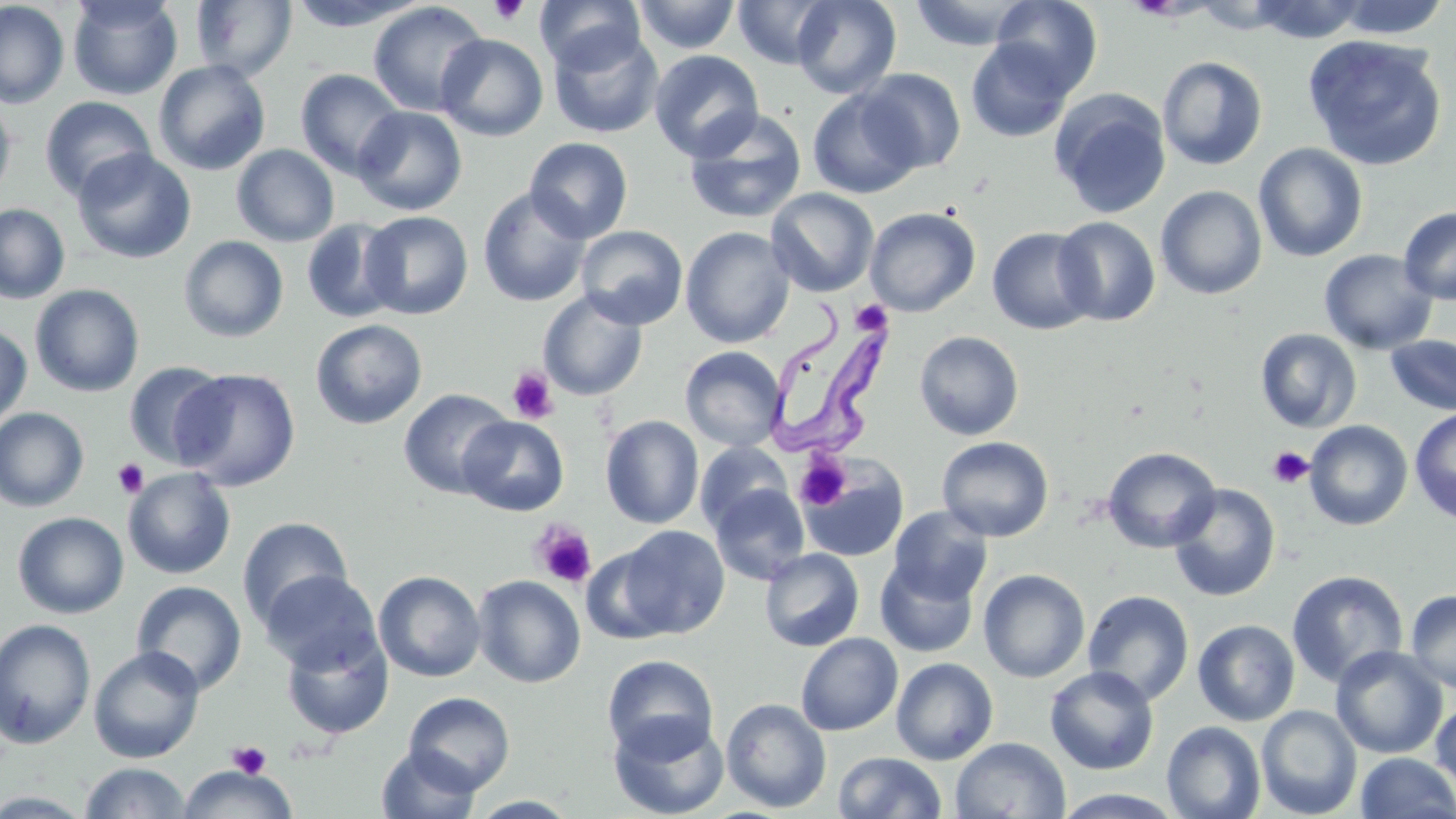

{
  "slide_level_diagnosis": "Trypanosoma brucei",
  "field_of_view": "one of a larger specimen",
  "stain": "May-Grünwald-Giemsa",
  "trypanosoma_brucei_locations": "approximate bounding boxes as named x1/y1/x2/y2 corners in pixels: (x1=768, y1=302, x2=894, y2=456)",
  "platelet_locations": "approximate bounding boxes as named x1/y1/x2/y2 corners in pixels: (x1=488, y1=0, x2=529, y2=25), (x1=850, y1=299, x2=893, y2=336), (x1=507, y1=368, x2=558, y2=423), (x1=1267, y1=446, x2=1314, y2=489), (x1=793, y1=453, x2=852, y2=511), (x1=112, y1=458, x2=150, y2=499), (x1=530, y1=521, x2=597, y2=589), (x1=227, y1=741, x2=271, y2=778)",
  "uninfected_red_blood_cell_locations": "approximate bounding boxes as named x1/y1/x2/y2 corners in pixels: (x1=67, y1=0, x2=183, y2=100), (x1=287, y1=0, x2=428, y2=31), (x1=535, y1=0, x2=645, y2=74), (x1=633, y1=0, x2=741, y2=54), (x1=732, y1=0, x2=837, y2=69), (x1=791, y1=0, x2=901, y2=98), (x1=991, y1=0, x2=1103, y2=96), (x1=1248, y1=0, x2=1369, y2=44), (x1=1333, y1=0, x2=1451, y2=40), (x1=0, y1=1, x2=70, y2=109), (x1=191, y1=1, x2=297, y2=82), (x1=908, y1=1, x2=1033, y2=50), (x1=368, y1=2, x2=489, y2=117), (x1=548, y1=26, x2=664, y2=139), (x1=436, y1=34, x2=548, y2=141), (x1=1302, y1=35, x2=1448, y2=170), (x1=965, y1=38, x2=1074, y2=143), (x1=649, y1=50, x2=764, y2=161), (x1=1157, y1=56, x2=1268, y2=170), (x1=153, y1=60, x2=271, y2=176), (x1=295, y1=69, x2=406, y2=180), (x1=857, y1=69, x2=967, y2=174), (x1=807, y1=88, x2=924, y2=199), (x1=1049, y1=89, x2=1172, y2=219), (x1=0, y1=95, x2=16, y2=201), (x1=39, y1=96, x2=156, y2=201), (x1=353, y1=106, x2=466, y2=215), (x1=683, y1=109, x2=808, y2=224), (x1=525, y1=137, x2=633, y2=243), (x1=1253, y1=143, x2=1369, y2=262), (x1=232, y1=144, x2=339, y2=247), (x1=72, y1=149, x2=196, y2=263), (x1=1155, y1=185, x2=1268, y2=300), (x1=477, y1=187, x2=591, y2=307), (x1=766, y1=188, x2=879, y2=297), (x1=0, y1=203, x2=70, y2=304), (x1=1399, y1=206, x2=1456, y2=304), (x1=864, y1=207, x2=980, y2=316), (x1=361, y1=211, x2=473, y2=320), (x1=1053, y1=215, x2=1161, y2=327), (x1=301, y1=218, x2=404, y2=324), (x1=576, y1=225, x2=688, y2=330), (x1=680, y1=227, x2=795, y2=348), (x1=987, y1=227, x2=1100, y2=335), (x1=179, y1=236, x2=289, y2=342), (x1=1319, y1=249, x2=1438, y2=354), (x1=30, y1=284, x2=145, y2=397), (x1=537, y1=290, x2=648, y2=401), (x1=311, y1=319, x2=428, y2=430), (x1=0, y1=323, x2=32, y2=430), (x1=1254, y1=328, x2=1362, y2=433), (x1=914, y1=331, x2=1024, y2=441), (x1=1385, y1=333, x2=1456, y2=416), (x1=680, y1=346, x2=787, y2=452), (x1=123, y1=362, x2=231, y2=469), (x1=172, y1=367, x2=301, y2=491), (x1=398, y1=389, x2=515, y2=499), (x1=0, y1=408, x2=90, y2=512), (x1=1409, y1=408, x2=1456, y2=524), (x1=458, y1=415, x2=569, y2=516), (x1=601, y1=415, x2=704, y2=529), (x1=1303, y1=420, x2=1413, y2=530), (x1=937, y1=436, x2=1054, y2=542), (x1=695, y1=442, x2=792, y2=532), (x1=1102, y1=446, x2=1222, y2=553), (x1=800, y1=458, x2=908, y2=563), (x1=122, y1=468, x2=236, y2=579), (x1=1168, y1=483, x2=1281, y2=603), (x1=709, y1=484, x2=810, y2=585), (x1=888, y1=506, x2=993, y2=605), (x1=13, y1=511, x2=129, y2=619), (x1=237, y1=516, x2=354, y2=631), (x1=611, y1=525, x2=730, y2=639), (x1=760, y1=548, x2=864, y2=651), (x1=875, y1=559, x2=979, y2=658), (x1=259, y1=569, x2=382, y2=673), (x1=978, y1=569, x2=1090, y2=683), (x1=1286, y1=569, x2=1409, y2=689), (x1=373, y1=570, x2=486, y2=682), (x1=473, y1=575, x2=586, y2=688), (x1=131, y1=580, x2=247, y2=696), (x1=1404, y1=588, x2=1456, y2=694), (x1=1082, y1=590, x2=1195, y2=705), (x1=0, y1=618, x2=96, y2=749), (x1=1192, y1=619, x2=1301, y2=726), (x1=280, y1=626, x2=394, y2=740), (x1=796, y1=633, x2=903, y2=735), (x1=89, y1=645, x2=205, y2=763), (x1=1331, y1=646, x2=1448, y2=759), (x1=601, y1=654, x2=719, y2=761), (x1=891, y1=657, x2=999, y2=765), (x1=1044, y1=666, x2=1159, y2=774), (x1=403, y1=691, x2=515, y2=794), (x1=1431, y1=696, x2=1456, y2=792), (x1=721, y1=698, x2=832, y2=813), (x1=1256, y1=705, x2=1362, y2=818), (x1=608, y1=713, x2=729, y2=819), (x1=1162, y1=720, x2=1266, y2=819), (x1=950, y1=736, x2=1070, y2=819), (x1=376, y1=746, x2=481, y2=819), (x1=833, y1=751, x2=947, y2=818), (x1=1355, y1=752, x2=1455, y2=818), (x1=80, y1=761, x2=192, y2=818), (x1=178, y1=767, x2=298, y2=819), (x1=1048, y1=788, x2=1189, y2=818), (x1=467, y1=795, x2=581, y2=817)",
  "magnification": "1000x",
  "image_size": "1456×819 pixels",
  "preparation": "thin blood film",
  "modality": "light microscopy"
}